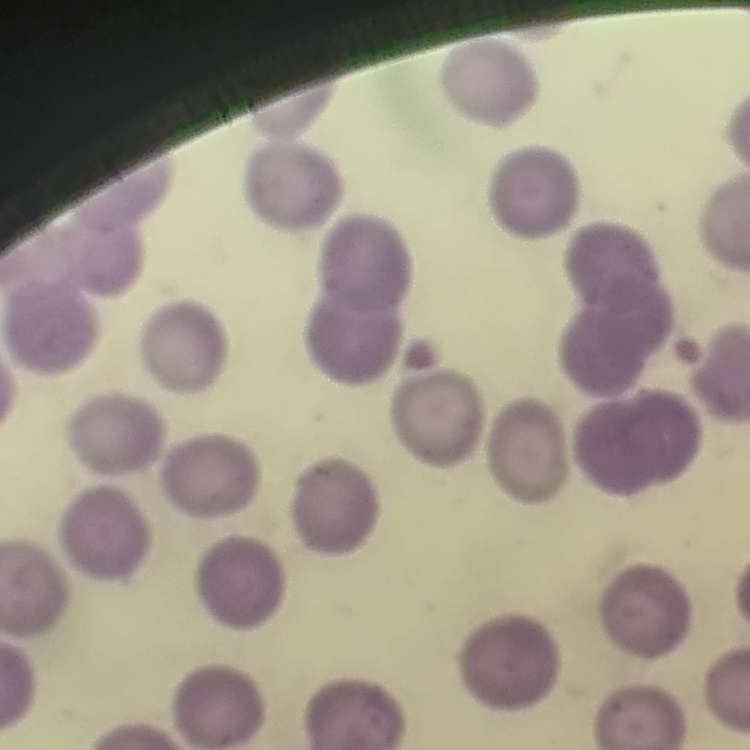

red blood cell morphology = no rouleaux formation
preparation = thin peripheral smear
image type = one tile cut from a larger photomicrograph
stain = Field's or Giemsa